Classify this cell by malaria status.
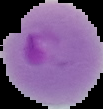

Parasitized.

From a thin blood film. Image is 103×109 pixels. Segmented cell region on a black background.